Describe the morphology of the erythrocytes.
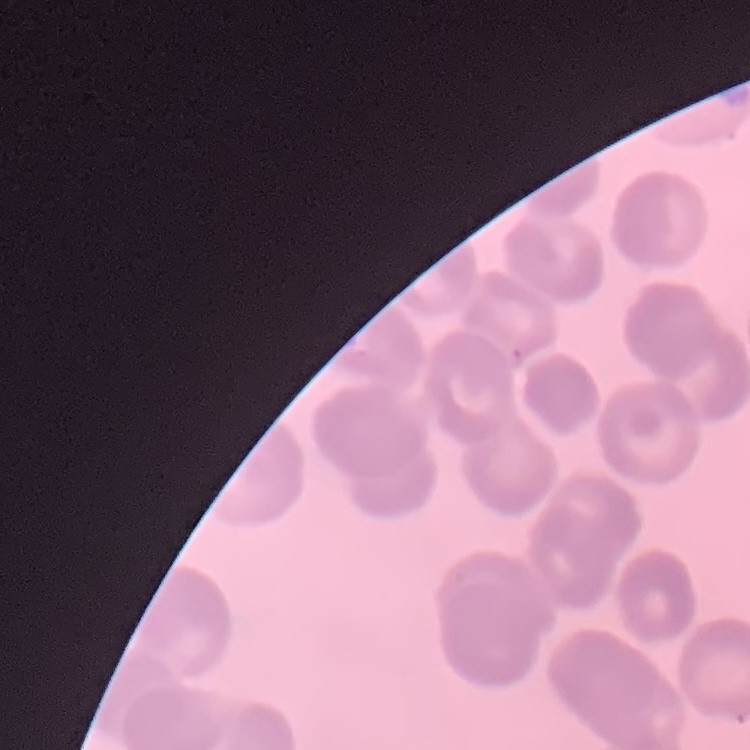
No rouleaux formation.

Summary:
  - Image type: one tile cut from a larger photomicrograph
  - Preparation: thin blood film
  - Stain: Field's or Giemsa